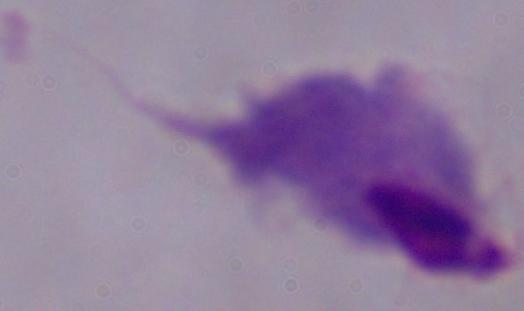
Photomicrograph. Captured at 1000x magnification. A trichomonad is shown.